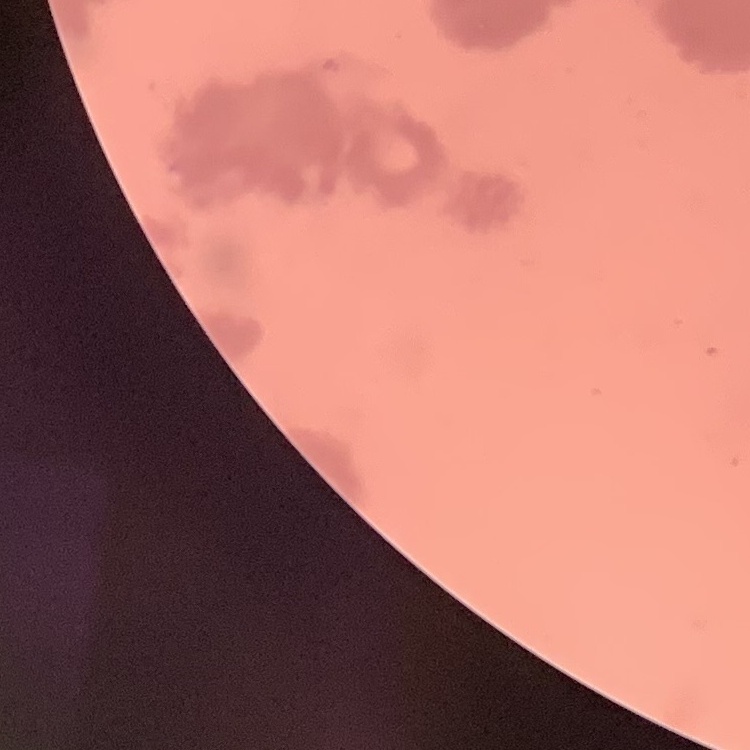
erythrocyte morphology = rouleaux formation
image type = square crop of a larger photomicrograph
preparation = thin blood smear
stain = Field's or Giemsa